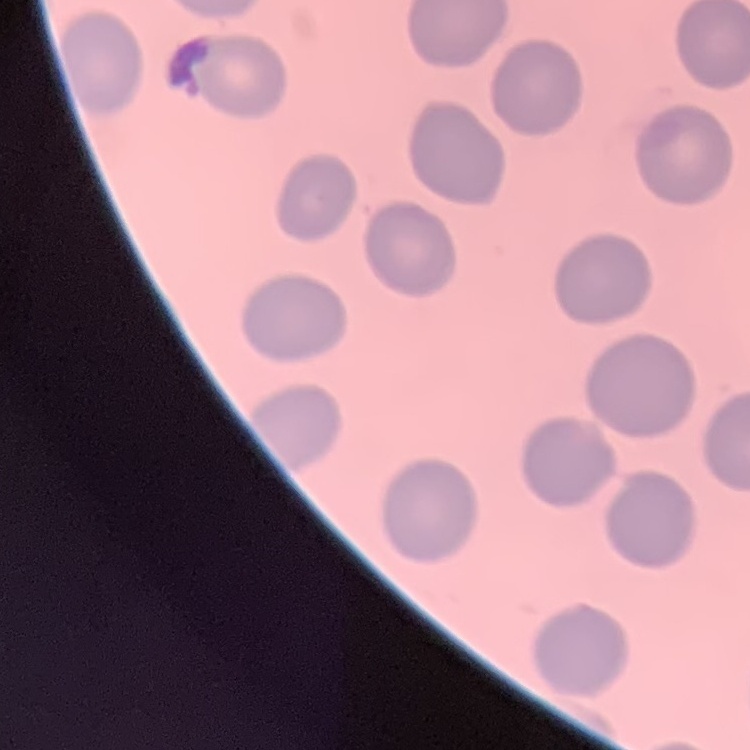

{
  "red_blood_cell_morphology": "no rouleaux formation",
  "image_type": "square crop of a larger photomicrograph",
  "preparation": "thin blood film",
  "stain": "Field's or Giemsa"
}